Name the cell type shown.
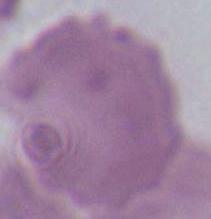

An erythrocyte.

Summary:
  - Magnification: 1000x
  - Modality: photomicrograph